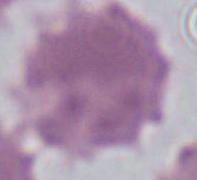

Summary:
  - Identification: red blood cell
  - Modality: micrograph
  - Magnification: 1000x